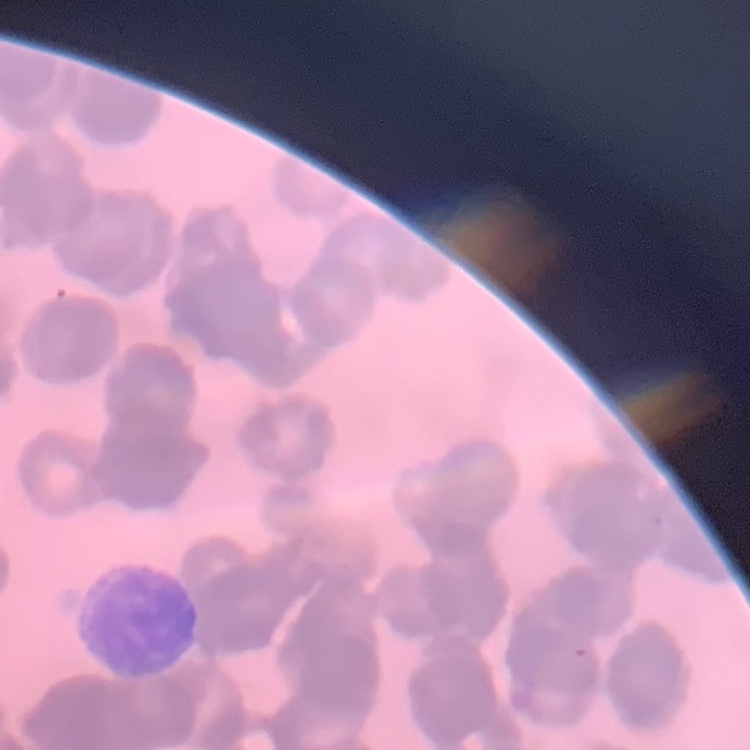 The red blood cells show rouleaux formation. Square crop of a larger photomicrograph. Stained with either Field's or Giemsa. Thin blood smear.